Name the parasite shown.
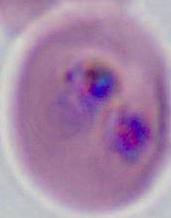

Plasmodium.

Summary:
  - Modality: micrograph
  - Magnification: 400x or 1000x